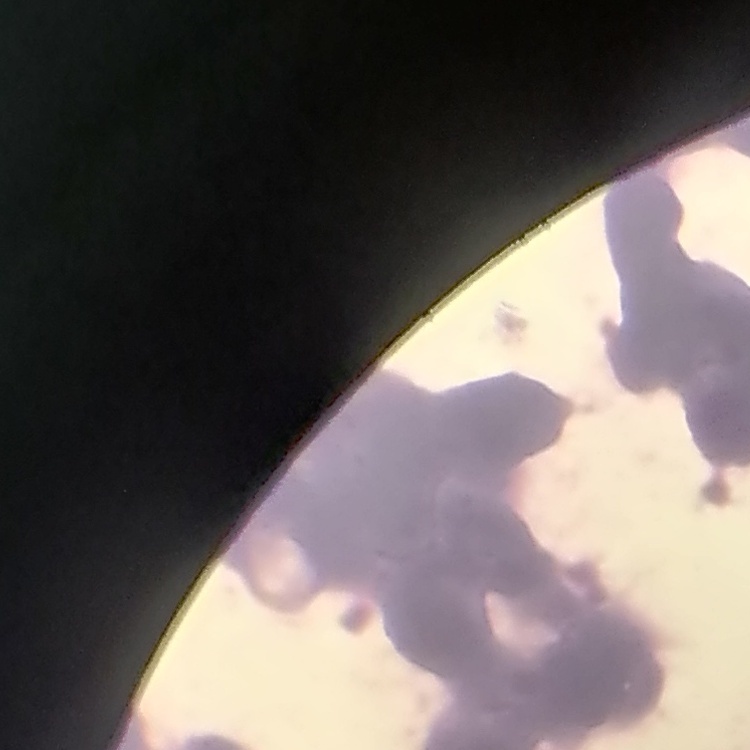 The red blood cells show rouleaux formation. Field's or Giemsa stain. Thin peripheral smear. One tile cut from a larger photomicrograph.